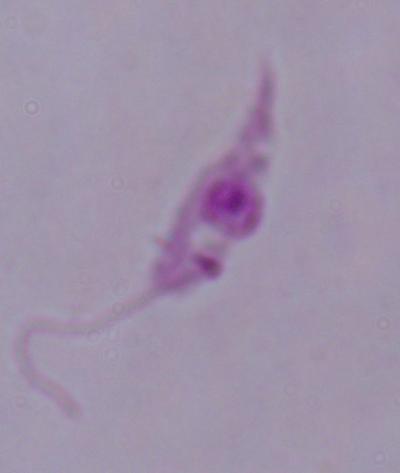

A Leishmania parasite is seen. Photomicrograph. Captured at 1000x magnification.